Assess this cell for malaria.
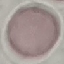

Uninfected.

{
  "image_type": "cell patch, automatically extracted from a larger field of view and resized to 64 × 64 pixels",
  "stain": "Giemsa",
  "capture": "smartphone through the microscope eyepiece",
  "preparation": "thin blood smear"
}